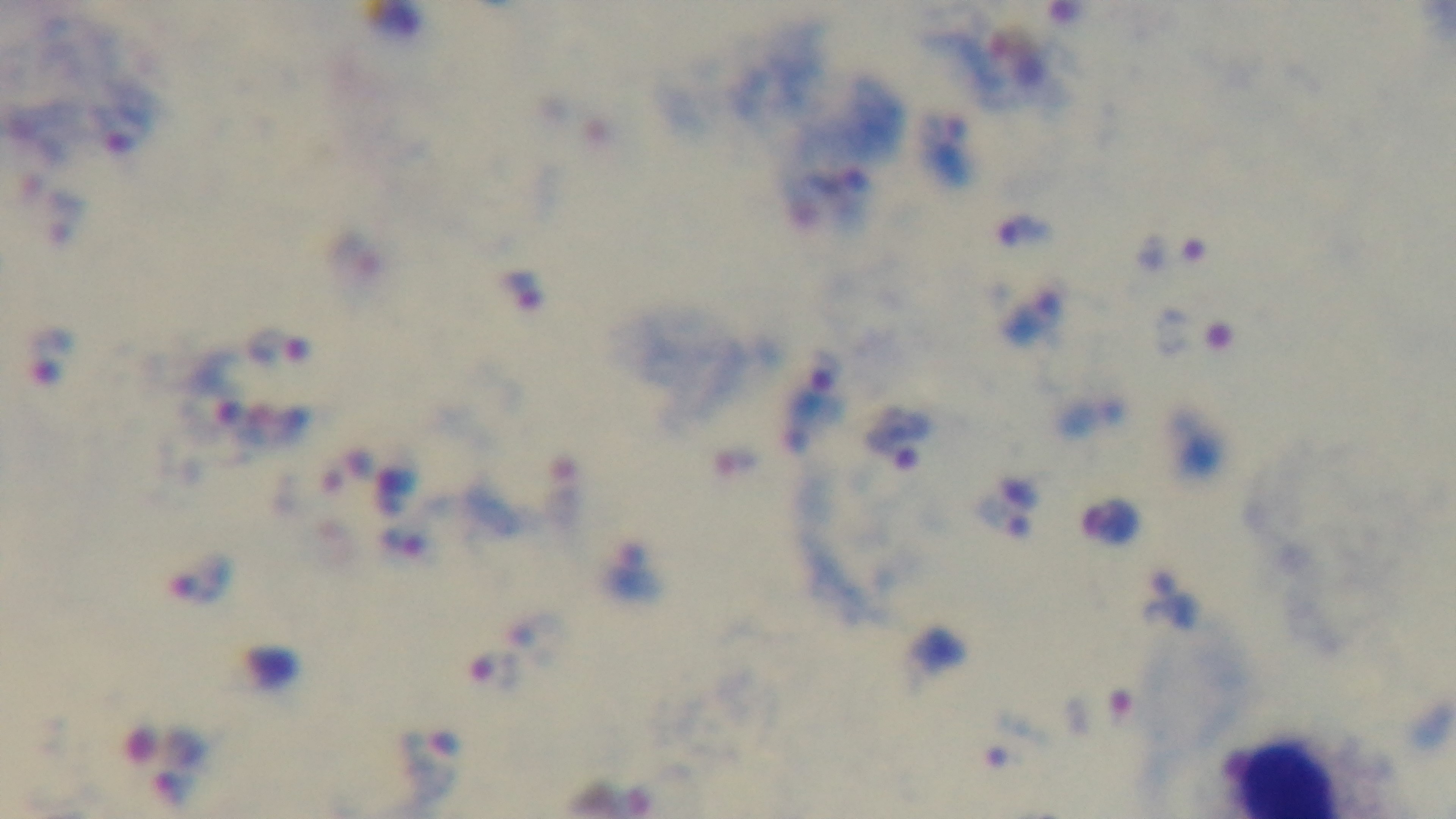

Summary:
  - Malaria status: infected
  - Objective: 100x oil immersion
  - Stain: Giemsa
  - Preparation: thick smear
  - Modality: light microscopy
  - Capture: mounted 4K digital camera
  - Field of view: single